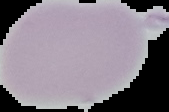 From a thin blood film. Result: no malaria parasites seen. The area outside the segmented cell region is set to black. Image is 169×112 pixels.